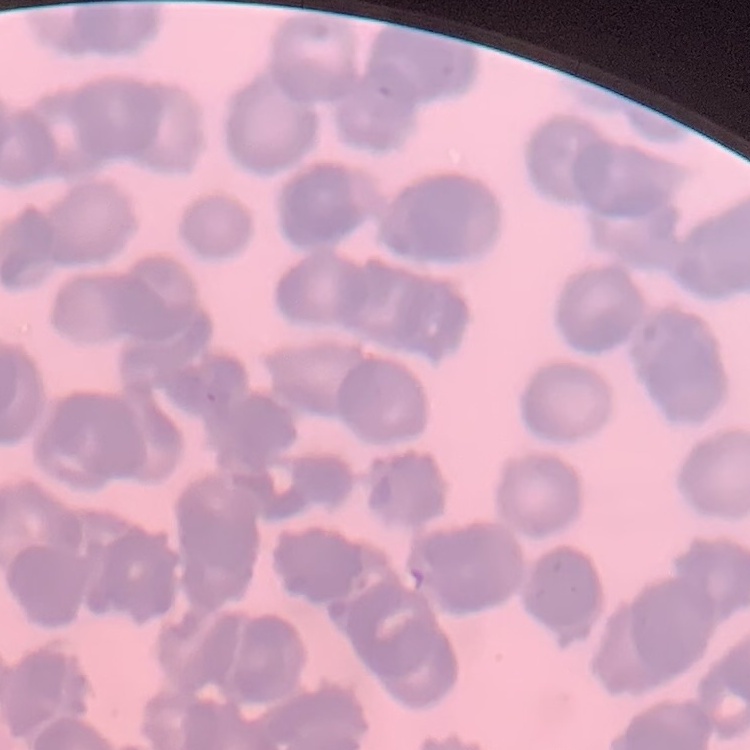

erythrocyte morphology = rouleaux formation
stain = Field's or Giemsa
preparation = thin blood film
image type = square crop of a larger photomicrograph